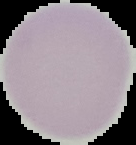
Image is 136×145 pixels. From a thin blood smear. Malaria status: uninfected. Cell region segmented out of the field of view; the surrounding area is masked to black.